Give a bounding box for every Plasmodium parasite.
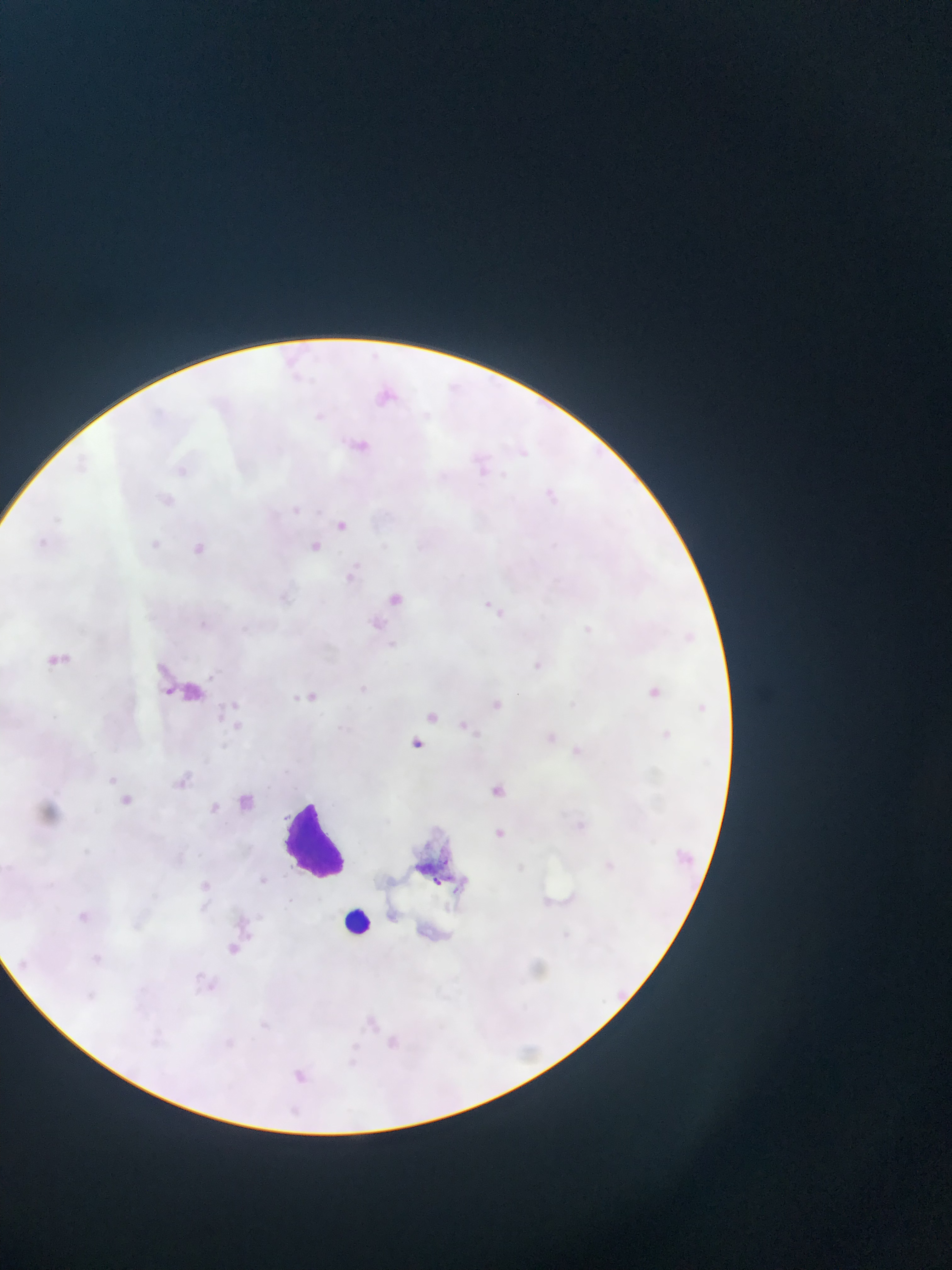
Approximate bounding boxes as {left, top, right, bottom} in pixels.
Plasmodium parasites: {371, 383, 401, 413}, {349, 436, 372, 458}, {510, 442, 532, 463}, {467, 448, 497, 481}, {167, 458, 193, 487}, {540, 487, 565, 511}, {154, 489, 181, 513}, {286, 504, 304, 520}, {330, 516, 353, 537}, {187, 536, 215, 564}, {305, 537, 325, 557}, {339, 559, 366, 588}, {381, 586, 410, 612}, {478, 598, 511, 627}, {574, 619, 600, 643}, {40, 645, 77, 679}, {525, 653, 548, 677}, {640, 682, 666, 706}, {289, 683, 321, 710}, {485, 693, 510, 717}, {421, 704, 445, 727}, {453, 715, 476, 738}, {654, 724, 679, 747}, {539, 726, 562, 750}, {404, 733, 430, 757}, {564, 739, 588, 763}, {169, 771, 196, 798}, {482, 779, 511, 805}, {114, 789, 137, 813}, {233, 790, 258, 816}, {203, 795, 226, 819}, {488, 823, 511, 844}, {669, 842, 703, 873}, {253, 871, 272, 890}, {192, 873, 218, 898}, {67, 902, 98, 931}, {220, 937, 246, 962}, {86, 947, 110, 971}, {356, 1008, 384, 1037}, {377, 1026, 409, 1059}, {282, 1060, 316, 1090}, {282, 1101, 304, 1120}.

Summary:
  - Artifact (stain precipitate or debris) locations: {149, 652, 228, 718}, {407, 832, 500, 900}
  - Leukocyte locations: {281, 797, 357, 882}, {330, 896, 385, 948}
  - Capture: mobile-phone photograph through a microscope
  - Field of view: single
  - Country: Ghana
  - Preparation: thin blood smear
  - Image size: 952×1270 pixels